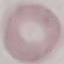
result: negative for malaria parasites
stain: Giemsa
capture: smartphone through the microscope eyepiece
image_type: automatically extracted cell patch, resized to 64 × 64 pixels
preparation: thin blood film